Assess this cell for malaria.
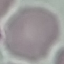

Uninfected.

stain: Giemsa
capture: smartphone camera at the microscope eyepiece
image_type: cell patch, automatically extracted from a larger field of view and resized to 64 × 64 pixels
preparation: thin smear